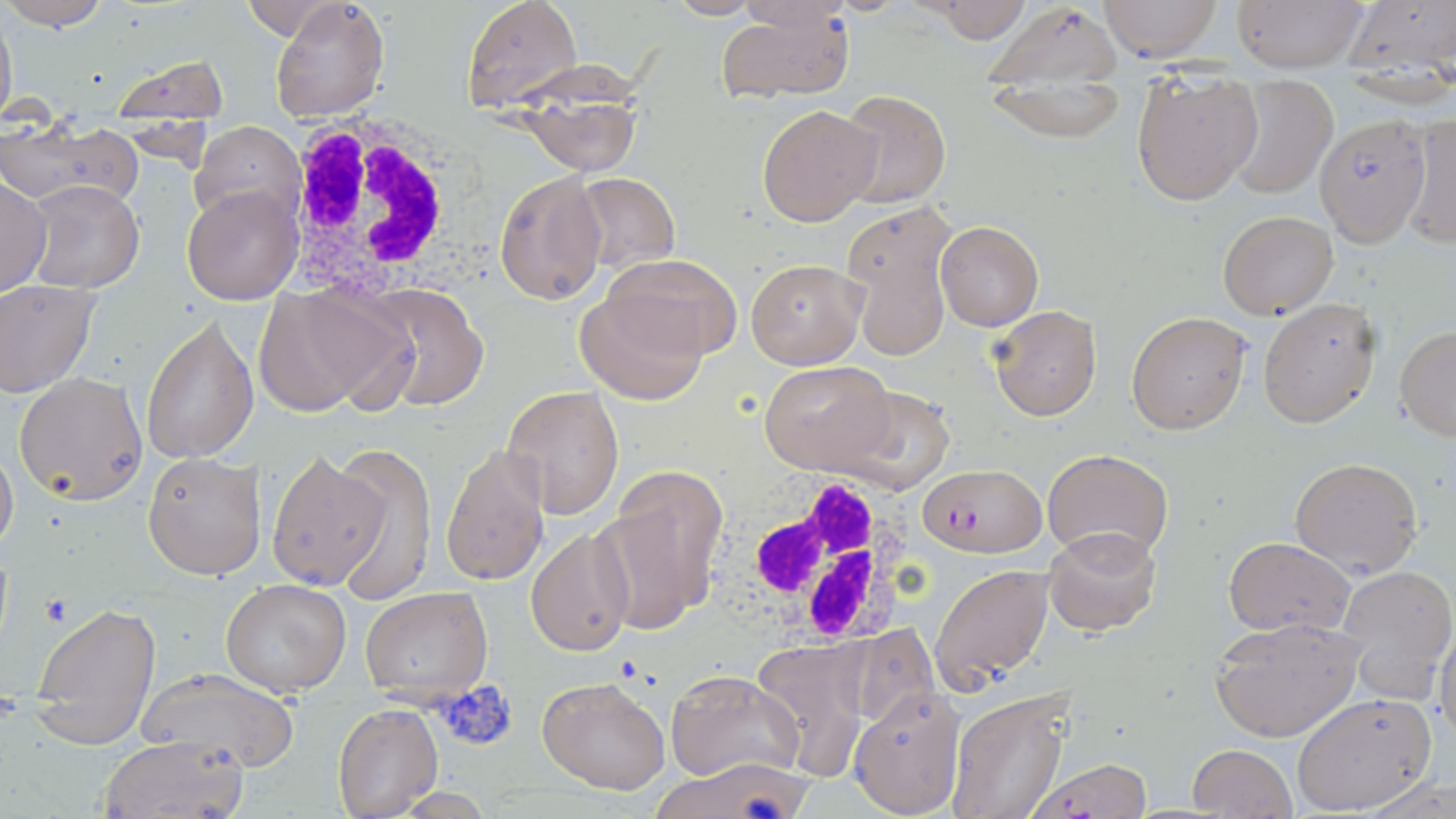
Approximate bounding boxes as (x1,y1)-(x2,y2) corner pairs in pixels. Plasmodium falciparum-infected red blood cell locations: (916,463)-(1042,556), (1025,757)-(1154,818). Uninfected red blood cell locations: (2,0)-(109,32), (268,0)-(391,123), (922,0)-(1034,44), (1098,0)-(1222,61), (1230,0)-(1369,72), (1338,0)-(1456,93), (461,1)-(580,111), (0,2)-(17,130), (987,5)-(1124,87), (715,6)-(855,102), (108,54)-(228,126), (513,58)-(658,178), (988,73)-(1129,143), (1130,73)-(1263,206), (1225,75)-(1340,199), (832,89)-(951,210), (757,102)-(883,226), (1400,113)-(1456,250), (1315,114)-(1431,246), (1,122)-(143,211), (190,122)-(304,228), (493,170)-(608,306), (573,173)-(682,274), (1,174)-(52,299), (24,180)-(144,294), (181,184)-(302,305), (840,202)-(956,359), (1218,209)-(1338,320), (935,220)-(1043,330), (606,255)-(741,360), (745,257)-(867,369), (0,281)-(99,397), (254,283)-(408,419), (357,284)-(493,411), (575,286)-(710,404), (1257,297)-(1382,428), (989,304)-(1103,421), (1126,311)-(1251,435), (141,316)-(259,465), (1394,327)-(1456,440), (760,359)-(893,476), (13,371)-(149,504), (829,381)-(959,494), (501,385)-(624,519), (0,439)-(19,559), (327,442)-(435,603), (442,443)-(551,588), (1043,448)-(1172,562), (265,449)-(389,592), (143,452)-(266,581), (1289,455)-(1424,576), (600,469)-(730,631), (1042,526)-(1161,638), (527,530)-(636,657), (1223,536)-(1352,637), (929,562)-(1055,694), (1334,562)-(1456,702), (220,579)-(352,697), (359,585)-(493,702), (27,602)-(162,748), (1210,616)-(1363,742), (1435,619)-(1456,747), (845,621)-(940,733), (754,639)-(869,782), (134,667)-(300,772), (668,669)-(804,783), (538,676)-(670,793), (849,687)-(966,817), (946,689)-(1073,819), (1291,691)-(1438,814), (332,703)-(443,818), (99,734)-(248,818), (1187,743)-(1297,819), (646,758)-(809,818), (1360,774)-(1455,818). White blood cell locations: (276,108)-(513,290), (710,469)-(925,650). Platelet locations: (41,595)-(74,628), (434,680)-(518,752). Slide-level diagnosis: Plasmodium falciparum. One field of a larger specimen. Image is 1456×819 pixels. 1000x magnification. Light microscopy. May-Grünwald-Giemsa stain. Thin blood smear.